State which parasite is depicted.
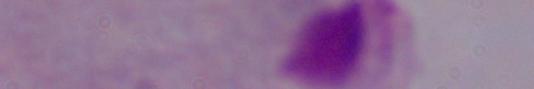
A trichomonad.

Captured at 1000x magnification. Micrograph.